Assess this cell for malaria.
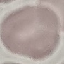
It is uninfected.

Automatically extracted cell patch, resized to 64 × 64 pixels. Photographed with a smartphone camera at the microscope eyepiece. Thin blood smear. Giemsa-stained preparation.